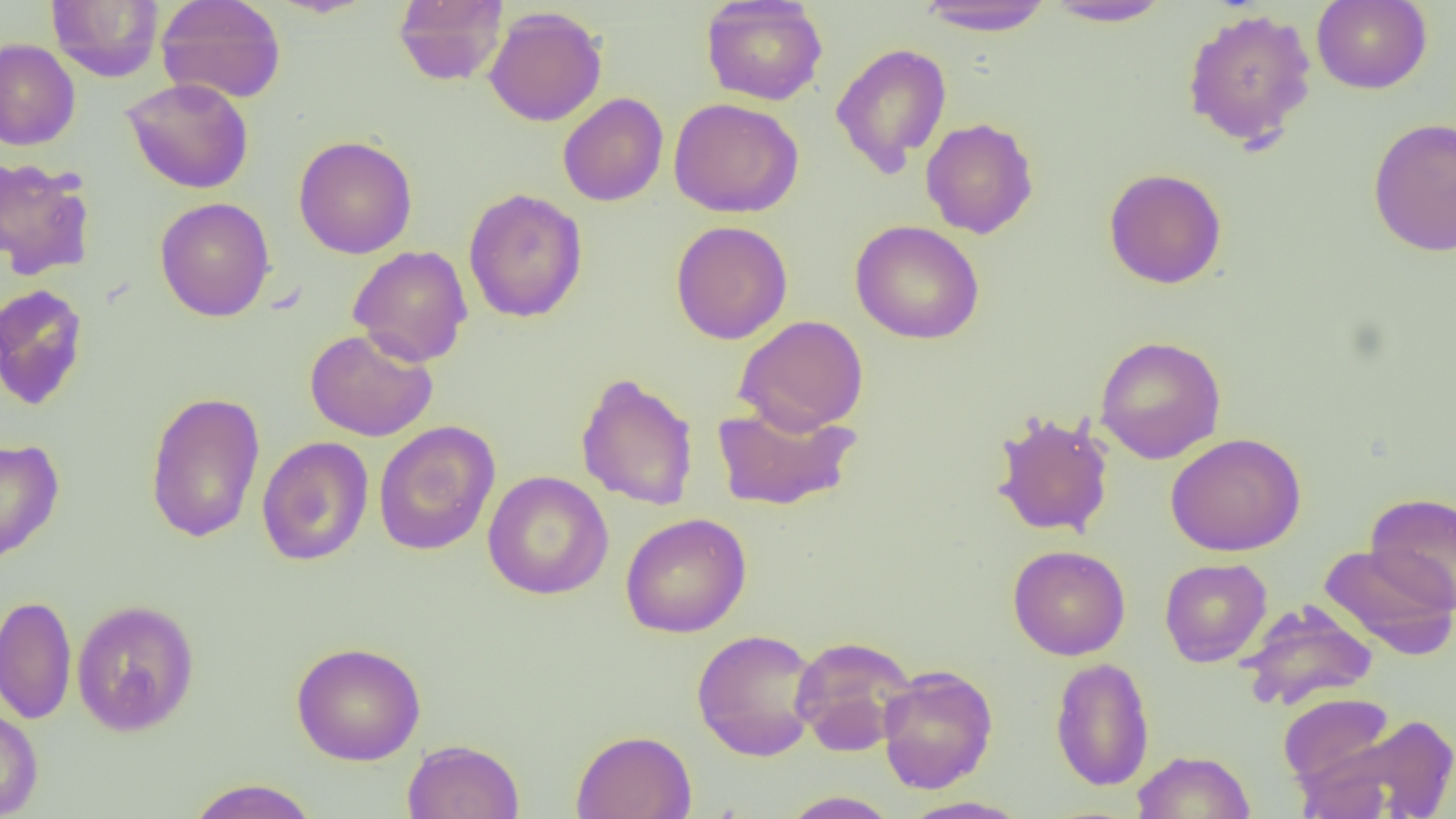

Summary:
  - Coordinate format: approximate bounding boxes as named x1/y1/x2/y2 corners in pixels
  - Uninfected red blood cell locations: (x1=47, y1=0, x2=165, y2=82), (x1=156, y1=0, x2=287, y2=104), (x1=393, y1=0, x2=508, y2=86), (x1=701, y1=0, x2=828, y2=106), (x1=1311, y1=0, x2=1432, y2=94), (x1=913, y1=1, x2=1056, y2=35), (x1=1042, y1=1, x2=1175, y2=27), (x1=484, y1=6, x2=608, y2=127), (x1=1181, y1=8, x2=1318, y2=148), (x1=0, y1=38, x2=81, y2=150), (x1=831, y1=42, x2=952, y2=176), (x1=122, y1=77, x2=254, y2=194), (x1=558, y1=92, x2=669, y2=207), (x1=668, y1=97, x2=804, y2=218), (x1=920, y1=117, x2=1039, y2=238), (x1=1368, y1=117, x2=1456, y2=257), (x1=293, y1=135, x2=417, y2=259), (x1=0, y1=157, x2=96, y2=281), (x1=1103, y1=168, x2=1228, y2=288), (x1=463, y1=188, x2=588, y2=323), (x1=155, y1=196, x2=276, y2=322), (x1=850, y1=219, x2=985, y2=344), (x1=670, y1=220, x2=793, y2=344), (x1=348, y1=245, x2=473, y2=367), (x1=0, y1=284, x2=89, y2=411), (x1=734, y1=314, x2=869, y2=435), (x1=304, y1=327, x2=438, y2=442), (x1=1095, y1=335, x2=1226, y2=464), (x1=576, y1=372, x2=699, y2=511), (x1=144, y1=391, x2=266, y2=544), (x1=711, y1=401, x2=861, y2=512), (x1=989, y1=410, x2=1115, y2=540), (x1=374, y1=420, x2=500, y2=556), (x1=1165, y1=432, x2=1306, y2=557), (x1=256, y1=435, x2=373, y2=566), (x1=0, y1=436, x2=64, y2=567), (x1=483, y1=470, x2=614, y2=600), (x1=1365, y1=492, x2=1456, y2=613), (x1=620, y1=512, x2=751, y2=638), (x1=1318, y1=543, x2=1456, y2=658), (x1=1007, y1=544, x2=1131, y2=660), (x1=1159, y1=557, x2=1272, y2=667), (x1=0, y1=594, x2=77, y2=725), (x1=71, y1=599, x2=200, y2=736), (x1=1238, y1=600, x2=1379, y2=711), (x1=691, y1=628, x2=822, y2=761), (x1=790, y1=635, x2=917, y2=755), (x1=291, y1=641, x2=427, y2=765), (x1=1050, y1=657, x2=1155, y2=792), (x1=877, y1=664, x2=998, y2=794), (x1=1277, y1=692, x2=1399, y2=791), (x1=0, y1=705, x2=43, y2=818), (x1=1325, y1=712, x2=1456, y2=818), (x1=570, y1=729, x2=697, y2=819), (x1=402, y1=739, x2=525, y2=819), (x1=1132, y1=750, x2=1256, y2=819), (x1=184, y1=779, x2=321, y2=819), (x1=780, y1=790, x2=901, y2=818), (x1=899, y1=796, x2=1031, y2=819)
  - Slide-level diagnosis: negative for blood parasites
  - Field of view: single
  - Magnification: 1000x
  - Modality: light microscopy
  - Preparation: thin blood film
  - Image size: 1456×819 pixels